Point out each Plasmodium parasite.
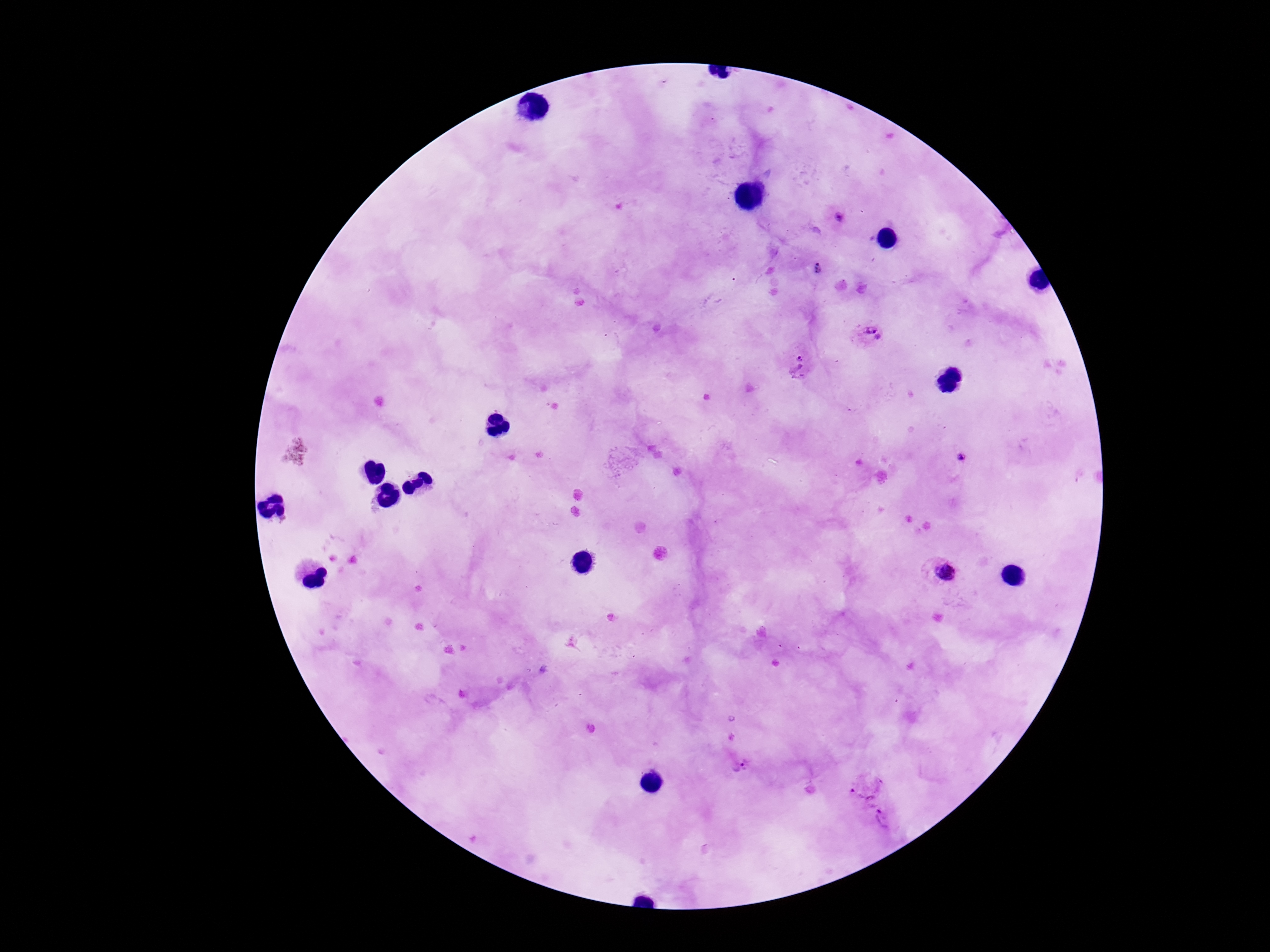

Approximate centers as [x, y] in pixels.
Plasmodium parasites: [841, 221], [816, 269], [868, 334], [798, 369], [945, 574], [744, 766], [863, 789], [882, 820].

preparation = thick blood film
capture = smartphone camera through the microscope eyepiece
magnification = 100x
image size = 1270×952 pixels
stain = Giemsa
patient malaria status = positive
field of view = single